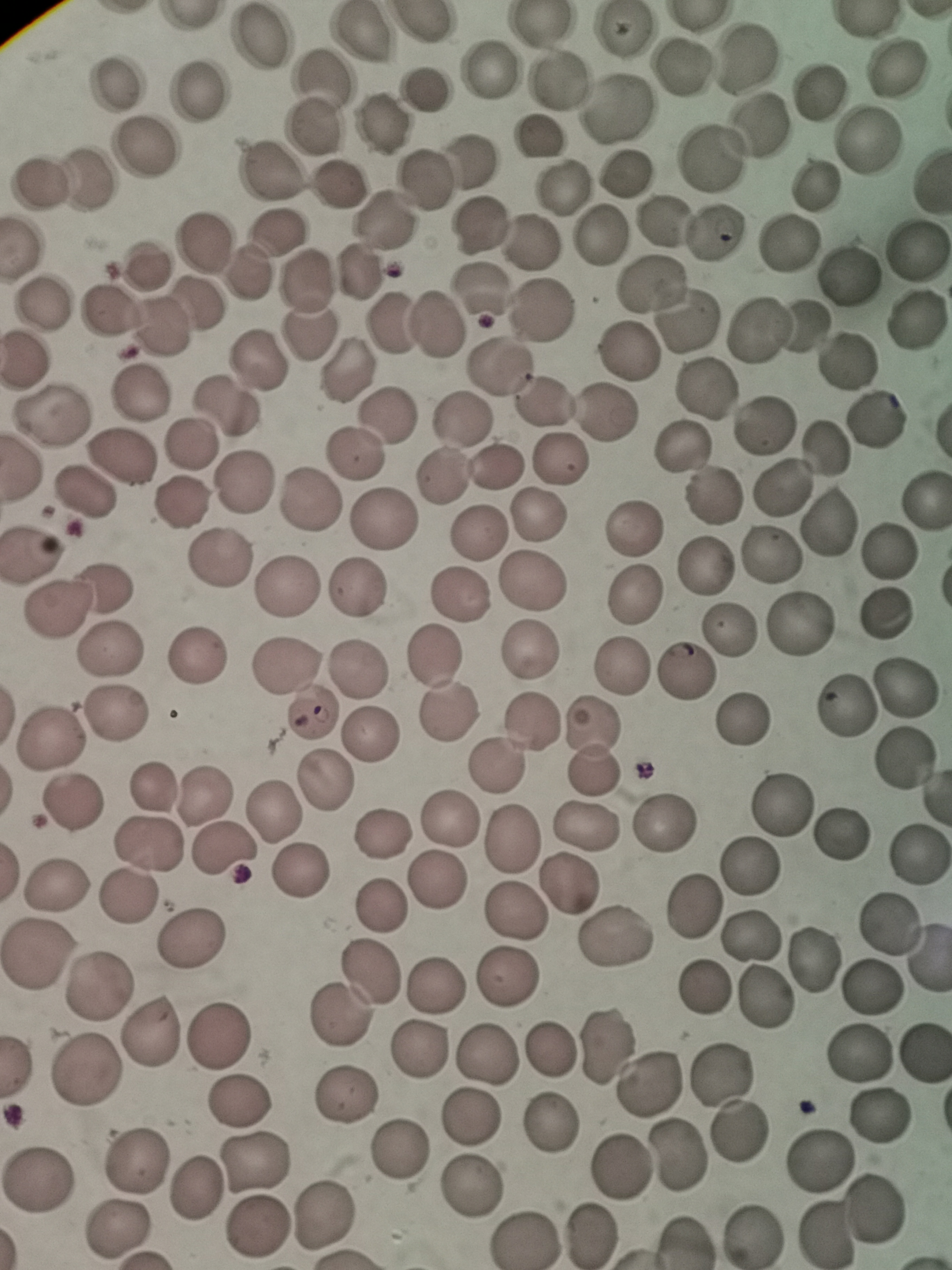
Approximate centers as [x, y] in pixels. Cell locations: [624, 30], [360, 35], [259, 37], [746, 57], [680, 65], [489, 69], [898, 69], [322, 75], [557, 80], [114, 82], [426, 89], [820, 90], [198, 93], [616, 106], [380, 123], [755, 126], [313, 127], [539, 140], [871, 140], [144, 145], [712, 160], [473, 161], [272, 173], [625, 174], [83, 179], [420, 180], [37, 183], [339, 184], [821, 186], [562, 188], [386, 221], [657, 221], [477, 224], [714, 231], [274, 232], [601, 233], [529, 240], [206, 243], [790, 243], [917, 252], [147, 263], [245, 271], [355, 271], [849, 276], [308, 281], [650, 283], [479, 288], [45, 303], [198, 303], [548, 305], [107, 307], [916, 317], [394, 322], [686, 322], [435, 323], [162, 324], [758, 324], [801, 325], [307, 330], [629, 351], [845, 360], [257, 362], [25, 364], [500, 367], [346, 373], [706, 388], [140, 392], [544, 399], [229, 409], [607, 413], [49, 415], [388, 417], [877, 417], [462, 422], [766, 428], [686, 445], [194, 446], [823, 450], [357, 455], [124, 456], [499, 467], [440, 474], [245, 481], [783, 486], [83, 496], [719, 497], [924, 497], [183, 504], [308, 504], [539, 516], [827, 520], [382, 521], [631, 530], [478, 533], [887, 552], [769, 555], [31, 559], [217, 562], [703, 565], [530, 578], [286, 588], [106, 589], [352, 590], [459, 594], [634, 595], [58, 612], [884, 616], [801, 619], [728, 628], [529, 648], [110, 649], [196, 655], [434, 658], [358, 665], [285, 669], [624, 669], [687, 672], [906, 684], [841, 708], [310, 713], [115, 714], [446, 714], [743, 719], [529, 720], [372, 734], [51, 738], [592, 746], [902, 756], [497, 764], [324, 782], [156, 789], [206, 796], [71, 804], [781, 805], [273, 811], [449, 818], [667, 824], [583, 828], [381, 833], [838, 835], [511, 838], [145, 845], [226, 850], [918, 860], [749, 866], [301, 869], [436, 880], [55, 885], [565, 890], [128, 897], [696, 905], [380, 907], [513, 912], [889, 923], [752, 935], [613, 939], [193, 940], [38, 956], [369, 972], [505, 977], [434, 983], [99, 987], [875, 987], [704, 989], [763, 998], [340, 1015], [151, 1032], [218, 1036], [606, 1045], [550, 1048], [415, 1052], [488, 1054], [857, 1054], [921, 1054], [86, 1069], [722, 1074], [648, 1085], [344, 1100], [238, 1102], [880, 1114], [471, 1115], [553, 1123], [740, 1129], [401, 1149], [679, 1154], [817, 1161], [132, 1163], [256, 1164], [619, 1164], [39, 1182], [473, 1185], [194, 1190], [874, 1207], [323, 1216], [257, 1226], [116, 1232], [752, 1234], [822, 1234], [523, 1235], [588, 1235], [684, 1240]. Acquired by smartphone through the microscope eyepiece. Giemsa stain. Image is 952×1270 pixels. One field from this slide. Thin blood smear.